Outline each uninfected red blood cell.
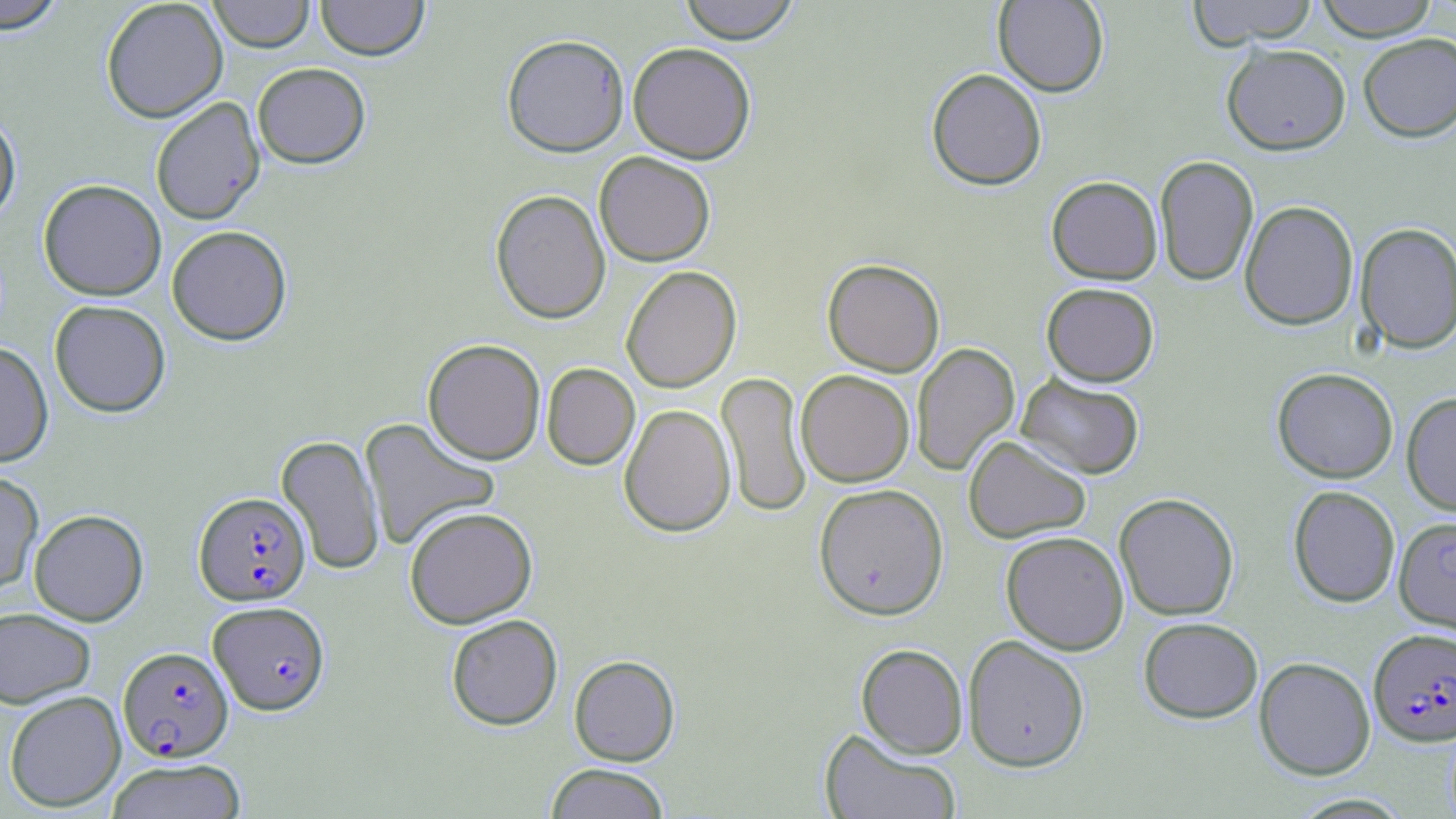

Approximate bounding boxes as named x1/y1/x2/y2 corners in pixels.
Uninfected red blood cells: (x1=0, y1=0, x2=69, y2=33), (x1=100, y1=0, x2=228, y2=123), (x1=208, y1=0, x2=315, y2=52), (x1=316, y1=0, x2=429, y2=61), (x1=678, y1=0, x2=802, y2=43), (x1=993, y1=0, x2=1109, y2=96), (x1=1187, y1=0, x2=1319, y2=47), (x1=1314, y1=0, x2=1440, y2=40), (x1=1358, y1=33, x2=1456, y2=142), (x1=501, y1=34, x2=630, y2=157), (x1=628, y1=41, x2=756, y2=164), (x1=1221, y1=43, x2=1351, y2=155), (x1=252, y1=62, x2=371, y2=168), (x1=926, y1=68, x2=1047, y2=190), (x1=150, y1=97, x2=265, y2=225), (x1=0, y1=108, x2=21, y2=225), (x1=594, y1=152, x2=716, y2=267), (x1=1154, y1=155, x2=1259, y2=286), (x1=1046, y1=175, x2=1162, y2=285), (x1=38, y1=179, x2=166, y2=300), (x1=490, y1=189, x2=611, y2=324), (x1=1239, y1=200, x2=1359, y2=330), (x1=1356, y1=221, x2=1456, y2=354), (x1=167, y1=225, x2=292, y2=345), (x1=822, y1=258, x2=945, y2=377), (x1=621, y1=266, x2=742, y2=393), (x1=1041, y1=282, x2=1159, y2=386), (x1=49, y1=299, x2=171, y2=417), (x1=423, y1=339, x2=545, y2=465), (x1=0, y1=341, x2=54, y2=467), (x1=911, y1=342, x2=1020, y2=477), (x1=541, y1=363, x2=640, y2=470), (x1=1272, y1=367, x2=1398, y2=483), (x1=795, y1=370, x2=914, y2=487), (x1=716, y1=371, x2=812, y2=518), (x1=1016, y1=373, x2=1145, y2=480), (x1=1401, y1=392, x2=1456, y2=517), (x1=619, y1=403, x2=736, y2=538), (x1=359, y1=417, x2=500, y2=551), (x1=276, y1=434, x2=385, y2=575), (x1=963, y1=435, x2=1091, y2=543), (x1=0, y1=469, x2=43, y2=593), (x1=813, y1=483, x2=949, y2=620), (x1=1288, y1=485, x2=1400, y2=607), (x1=1114, y1=492, x2=1239, y2=621), (x1=404, y1=506, x2=537, y2=629), (x1=29, y1=508, x2=148, y2=625), (x1=1000, y1=531, x2=1129, y2=654), (x1=0, y1=607, x2=95, y2=708), (x1=446, y1=614, x2=563, y2=730), (x1=1138, y1=617, x2=1263, y2=723), (x1=963, y1=634, x2=1090, y2=772), (x1=856, y1=643, x2=968, y2=758), (x1=569, y1=654, x2=680, y2=766), (x1=1254, y1=656, x2=1376, y2=780), (x1=4, y1=690, x2=126, y2=812), (x1=820, y1=729, x2=960, y2=818), (x1=106, y1=758, x2=247, y2=819), (x1=544, y1=763, x2=671, y2=818), (x1=1289, y1=793, x2=1413, y2=818).

Plasmodium falciparum-infected red blood cell locations: (x1=194, y1=492, x2=310, y2=605), (x1=1393, y1=516, x2=1456, y2=635), (x1=209, y1=601, x2=330, y2=714), (x1=1368, y1=627, x2=1456, y2=747), (x1=118, y1=646, x2=233, y2=762). Slide-level diagnosis: Plasmodium falciparum. Light microscopy. Single field of view. Image is 1456×819 pixels. Thin blood smear. Captured at 1000x magnification. May-Grünwald-Giemsa-stained preparation.